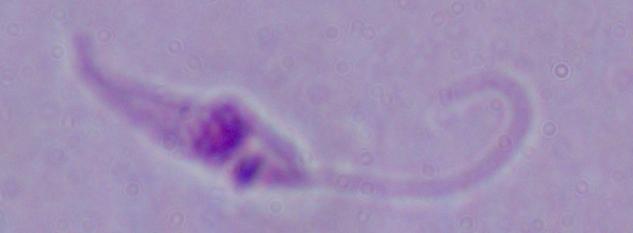 Captured at 1000x magnification. A Leishmania parasite is shown. Photomicrograph.